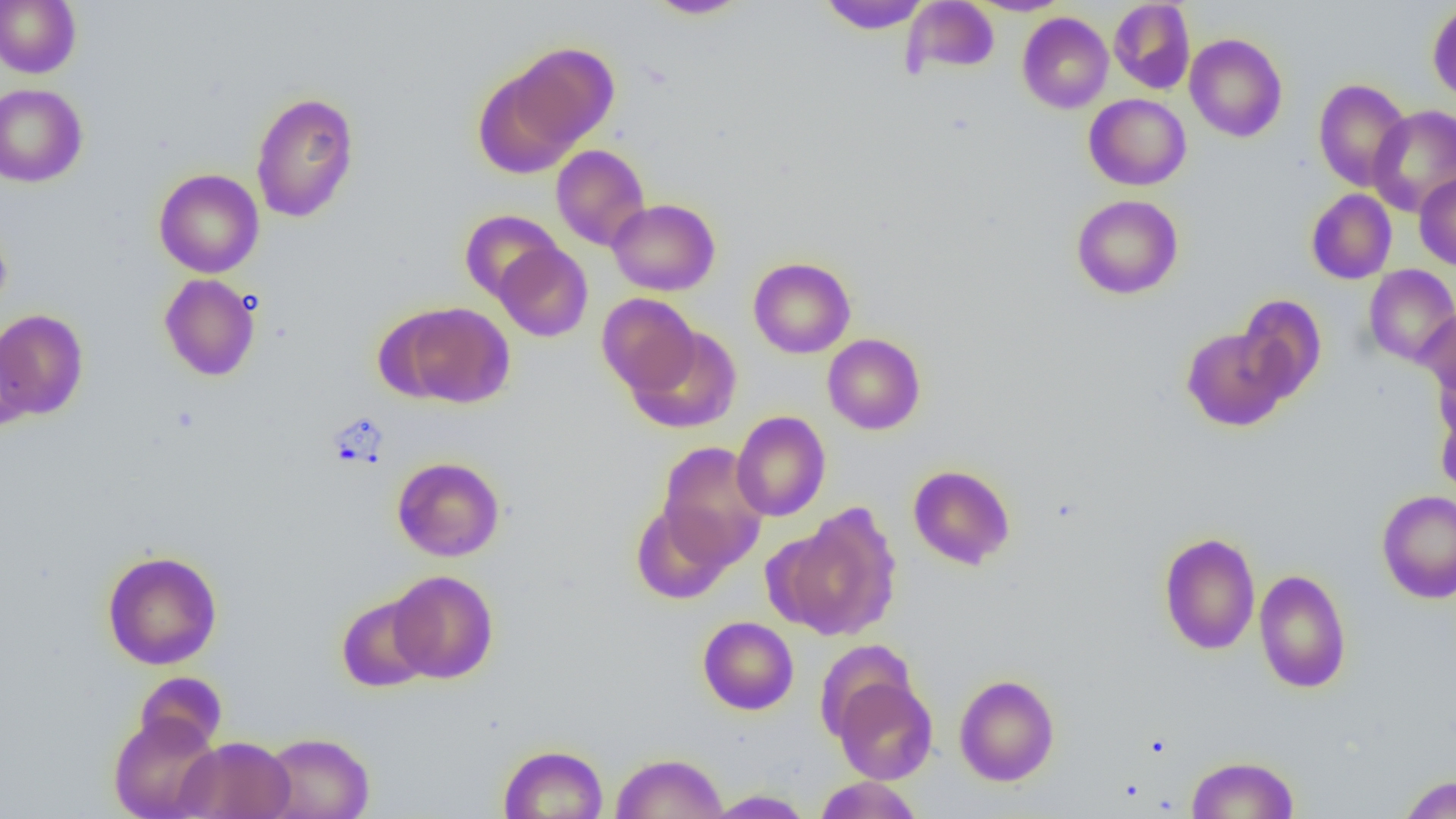

slide-level diagnosis = negative for blood parasites
modality = optical microscopy
magnification = 1000x
image size = 1456×819 pixels
field of view = single
preparation = thin blood smear
uninfected red blood cell locations = approximate bounding boxes as (x1,y1)-(x2,y2) corner pairs in pixels: (0,0)-(81,77), (646,0)-(751,19), (967,0)-(1072,16), (818,1)-(930,34), (903,1)-(999,76), (1109,1)-(1195,94), (1427,2)-(1456,104), (1017,12)-(1113,114), (1185,34)-(1288,142), (505,43)-(619,151), (472,64)-(585,179), (1313,79)-(1412,191), (0,83)-(88,187), (250,92)-(360,223), (1084,94)-(1191,190), (1368,105)-(1456,216), (551,144)-(650,251), (154,168)-(265,278), (1414,172)-(1456,270), (1306,188)-(1397,284), (1071,195)-(1183,299), (607,199)-(720,296), (459,210)-(562,302), (0,220)-(12,318), (494,242)-(593,342), (748,256)-(856,358), (1363,264)-(1456,367), (159,274)-(261,381), (597,293)-(700,395), (1237,294)-(1327,402), (392,302)-(515,408), (1417,306)-(1456,403), (0,309)-(88,419), (626,325)-(742,434), (1181,326)-(1293,431), (822,333)-(925,434), (2,338)-(34,432), (1431,352)-(1456,445), (1436,405)-(1456,499), (731,411)-(830,521), (657,442)-(767,567), (392,456)-(505,562), (908,464)-(1016,570), (1377,490)-(1456,604), (630,502)-(735,605), (777,505)-(902,641), (1158,532)-(1261,655), (102,550)-(222,670), (1253,569)-(1352,693), (388,571)-(498,683), (336,594)-(435,693), (698,616)-(798,714), (133,672)-(228,754), (832,674)-(937,784), (954,674)-(1059,786), (108,711)-(222,819), (261,732)-(375,819), (176,736)-(296,819), (498,744)-(609,819), (612,752)-(727,819), (1186,755)-(1299,818), (1399,775)-(1456,819), (814,776)-(924,818), (705,789)-(813,818)